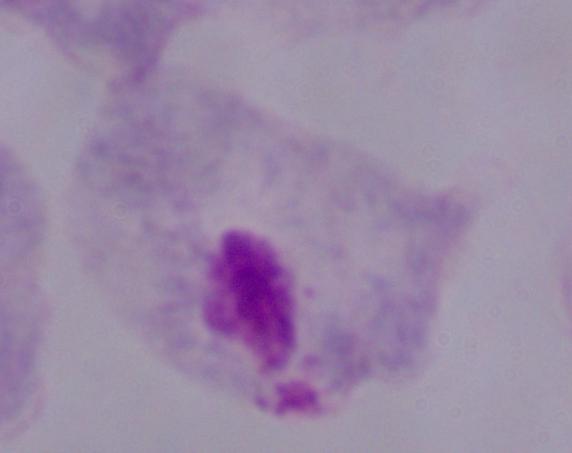

Summary:
  - Identification: trichomonad
  - Modality: photomicrograph
  - Magnification: 1000x